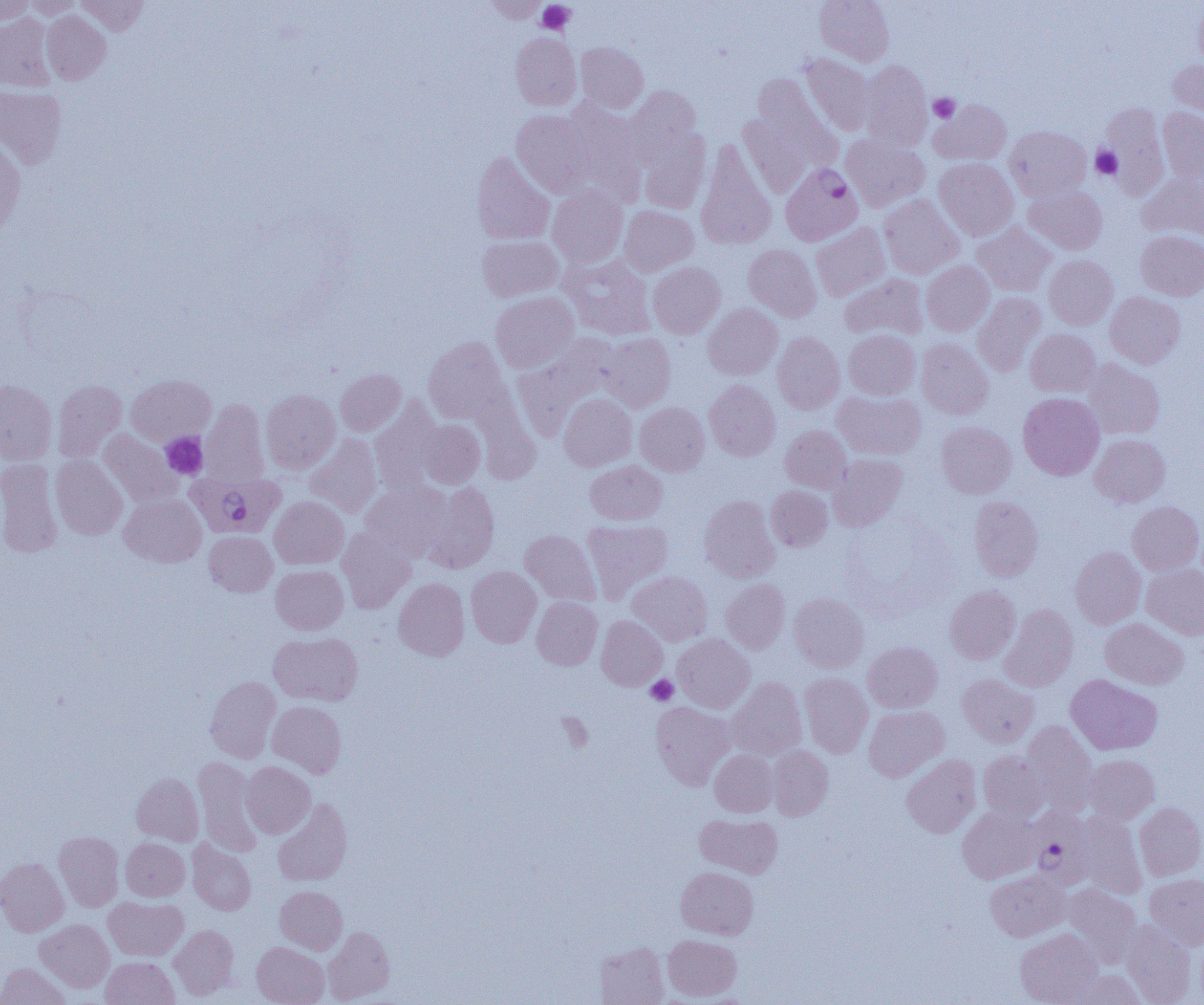

Summary:
  - Coordinate format: approximate bounding boxes as (x1, y1, x2, y2) in pixels
  - Plasmodium falciparum-infected red blood cell locations: (780, 163, 862, 246), (186, 471, 284, 539), (1026, 806, 1093, 888)
  - Platelet locations: (537, 1, 574, 35), (928, 93, 960, 123), (1091, 146, 1123, 180), (160, 432, 208, 479), (646, 675, 679, 706), (558, 712, 593, 752)
  - Uninfected red blood cell locations: (0, 0, 35, 25), (24, 0, 84, 18), (76, 0, 149, 35), (481, 0, 548, 23), (814, 0, 894, 66), (1194, 1, 1204, 72), (41, 11, 111, 85), (0, 13, 56, 91), (510, 33, 581, 110), (576, 42, 648, 113), (800, 53, 875, 136), (1168, 59, 1204, 118), (859, 60, 932, 151), (751, 73, 841, 166), (0, 86, 67, 169), (625, 86, 702, 165), (931, 99, 1011, 165), (562, 100, 645, 202), (1100, 104, 1169, 198), (1158, 107, 1204, 183), (512, 110, 594, 197), (738, 113, 814, 196), (1004, 126, 1091, 201), (638, 130, 711, 214), (841, 134, 930, 212), (0, 135, 26, 235), (696, 142, 776, 249), (472, 151, 554, 245), (934, 158, 1018, 241), (1138, 173, 1204, 241), (1024, 184, 1108, 254), (547, 185, 628, 268), (878, 194, 964, 278), (619, 205, 699, 276), (972, 222, 1056, 296), (811, 223, 890, 301), (1136, 230, 1204, 301), (478, 235, 563, 301), (744, 244, 822, 321), (560, 254, 658, 340), (1044, 255, 1118, 329), (921, 261, 994, 336), (648, 262, 725, 338), (839, 273, 928, 342), (491, 291, 579, 372), (1105, 292, 1185, 368), (972, 293, 1046, 376), (703, 303, 783, 380), (843, 329, 920, 400), (1025, 329, 1101, 397), (772, 332, 845, 414), (598, 333, 676, 412), (513, 334, 621, 435), (424, 337, 510, 424), (916, 338, 993, 419), (1083, 359, 1165, 439), (335, 369, 406, 436), (126, 375, 215, 445), (53, 379, 126, 461), (0, 380, 57, 465), (705, 380, 780, 460), (260, 390, 340, 474), (833, 390, 926, 460), (559, 393, 637, 471), (1018, 393, 1104, 480), (201, 399, 269, 486), (370, 400, 444, 493), (635, 402, 709, 476), (416, 419, 485, 488), (936, 421, 1016, 498), (780, 425, 851, 493), (98, 429, 183, 508), (305, 434, 382, 517), (1090, 434, 1169, 507), (827, 454, 907, 531), (51, 455, 128, 540), (0, 458, 63, 558), (585, 460, 667, 525), (361, 481, 453, 563), (421, 482, 500, 573), (765, 486, 832, 551), (119, 493, 206, 567), (269, 496, 349, 569), (699, 496, 780, 582), (969, 496, 1043, 581), (1127, 501, 1203, 575), (582, 518, 673, 601), (337, 528, 416, 613), (520, 530, 600, 606), (204, 531, 277, 596), (1070, 547, 1146, 628), (1142, 563, 1204, 639), (271, 565, 348, 635), (466, 566, 541, 647), (628, 571, 712, 645), (393, 577, 469, 660), (721, 578, 790, 654), (944, 585, 1021, 664), (789, 593, 869, 672), (531, 596, 603, 670), (1000, 604, 1078, 691), (597, 615, 668, 690), (1100, 617, 1189, 689), (268, 632, 363, 705), (673, 634, 755, 713), (863, 641, 943, 712), (799, 672, 873, 758), (957, 674, 1039, 747), (1066, 674, 1162, 755), (205, 676, 281, 763), (726, 677, 807, 760), (268, 701, 346, 778), (650, 702, 735, 790), (864, 705, 949, 781), (1022, 721, 1098, 814), (768, 746, 833, 820), (710, 750, 777, 817), (978, 751, 1049, 823), (901, 755, 981, 837), (1085, 755, 1159, 823), (193, 757, 262, 856), (241, 761, 315, 838), (131, 773, 204, 846), (273, 798, 352, 886), (1135, 802, 1204, 880), (957, 807, 1040, 883), (1077, 811, 1147, 899), (695, 814, 783, 878), (54, 831, 124, 911), (121, 838, 189, 901), (187, 840, 256, 915), (0, 858, 69, 936), (676, 866, 758, 939), (986, 870, 1070, 941), (1145, 873, 1204, 950), (1062, 884, 1141, 966), (275, 886, 347, 954), (104, 896, 187, 960), (1121, 919, 1197, 1005), (35, 920, 114, 992), (169, 925, 239, 999), (323, 926, 395, 1003), (1015, 929, 1102, 1005), (663, 934, 742, 1000), (1195, 938, 1204, 1005), (252, 941, 329, 1005), (597, 942, 669, 1005), (101, 957, 179, 1005), (0, 962, 71, 1005), (1069, 970, 1146, 1004)
  - Slide-level diagnosis: Plasmodium falciparum
  - Image size: 1204×1005 pixels
  - Preparation: thin blood film
  - Field of view: one of a larger specimen
  - Modality: optical microscopy
  - Magnification: 1000x